Describe the morphology of the erythrocytes.
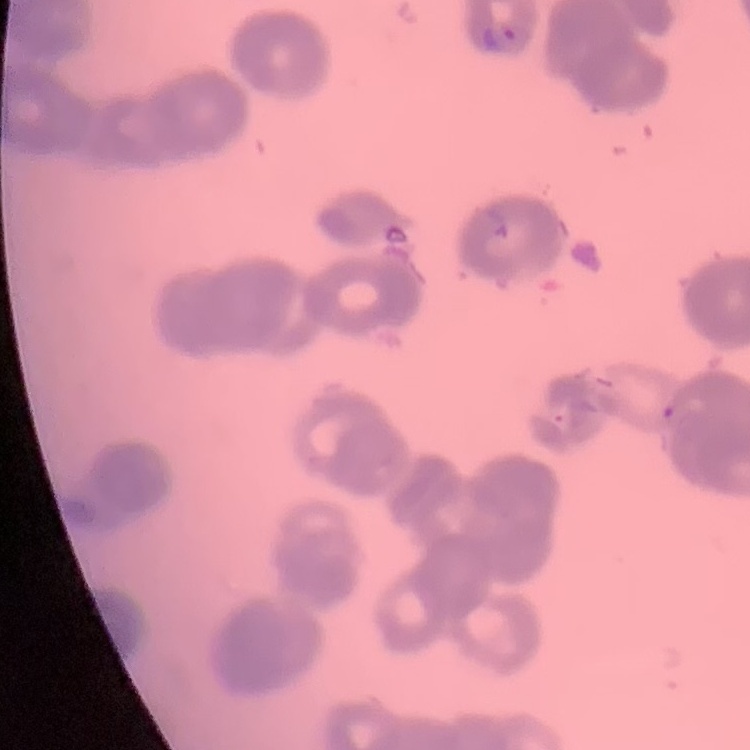
Rouleaux formation.

Field's or Giemsa stain. Square crop of a larger photomicrograph. Thin peripheral smear.